Assess the morphology of the erythrocytes.
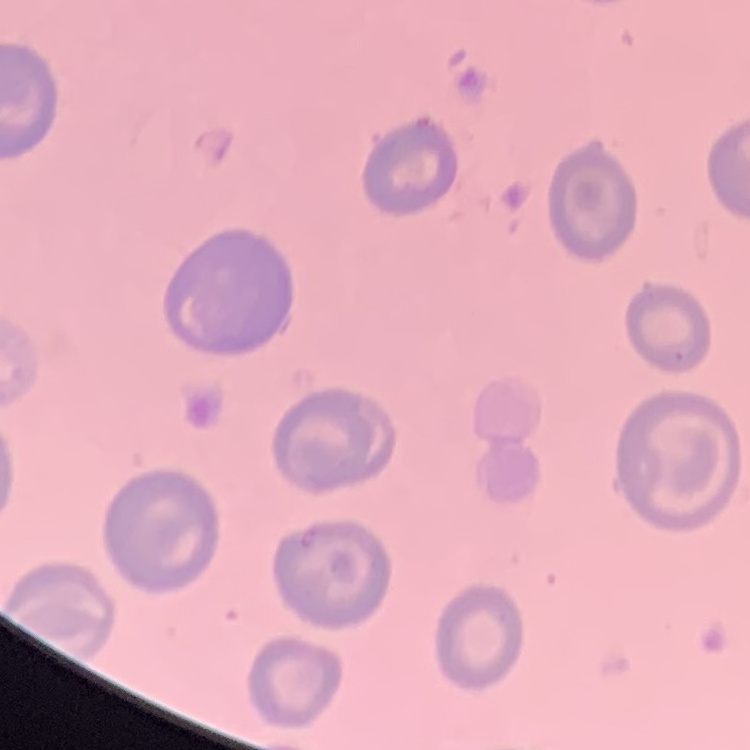

No rouleaux formation.

Summary:
  - Preparation: thin peripheral smear
  - Stain: Field's or Giemsa
  - Image type: one tile cut from a larger photomicrograph